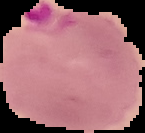

From a thin blood smear. Cell region segmented out of the field of view; the surrounding area is masked to black. Malaria status: parasitized. Image is 145×133 pixels.